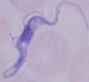

Summary:
  - Magnification: 1000x
  - Modality: photomicrograph
  - Identification: trypanosome